State the preparation type.
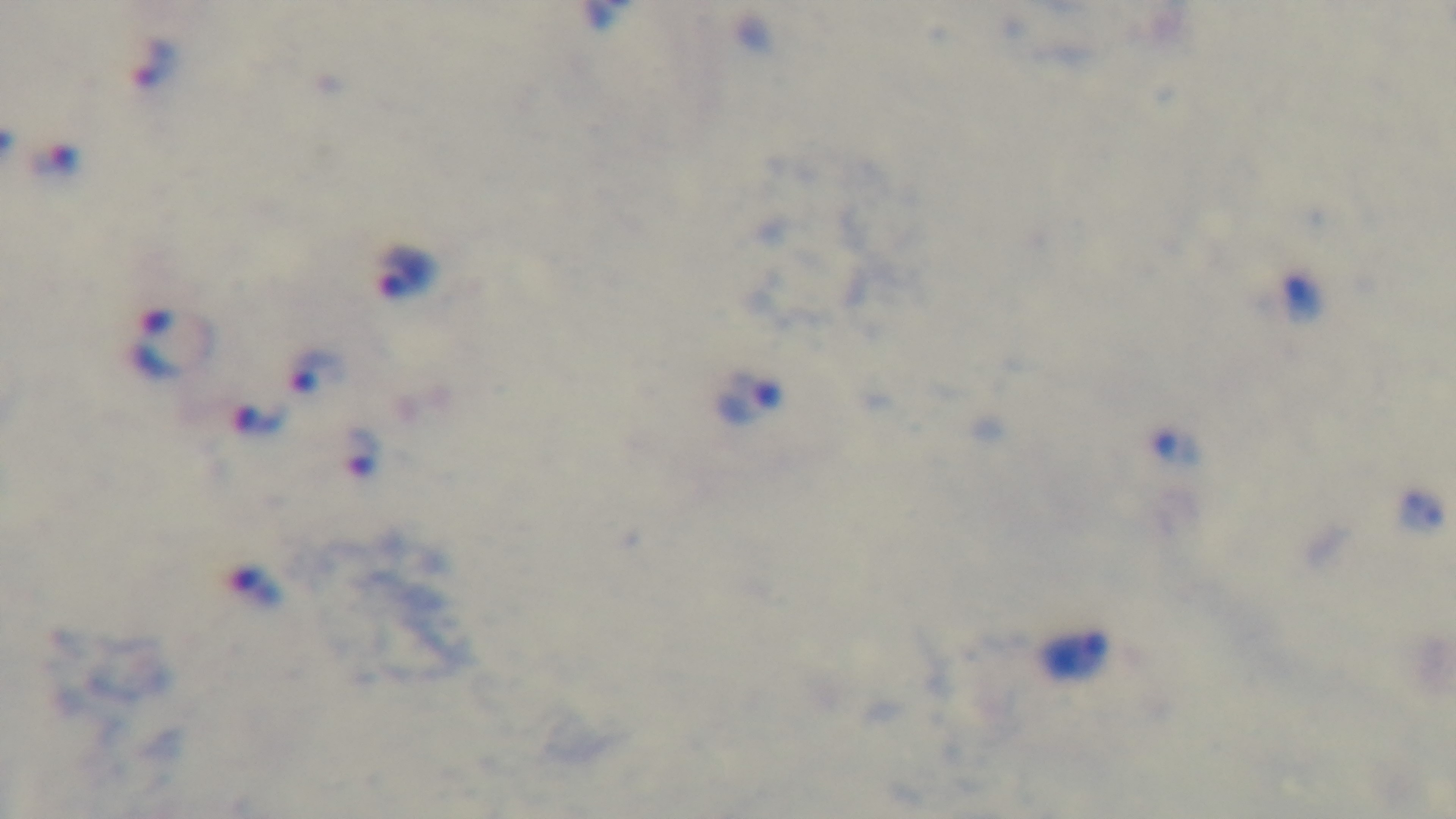
A thick smear.

field of view = one from the slide
malaria status = infected
stain = Giemsa
modality = light microscopy
capture = mounted 4K digital camera
objective = 100x oil immersion